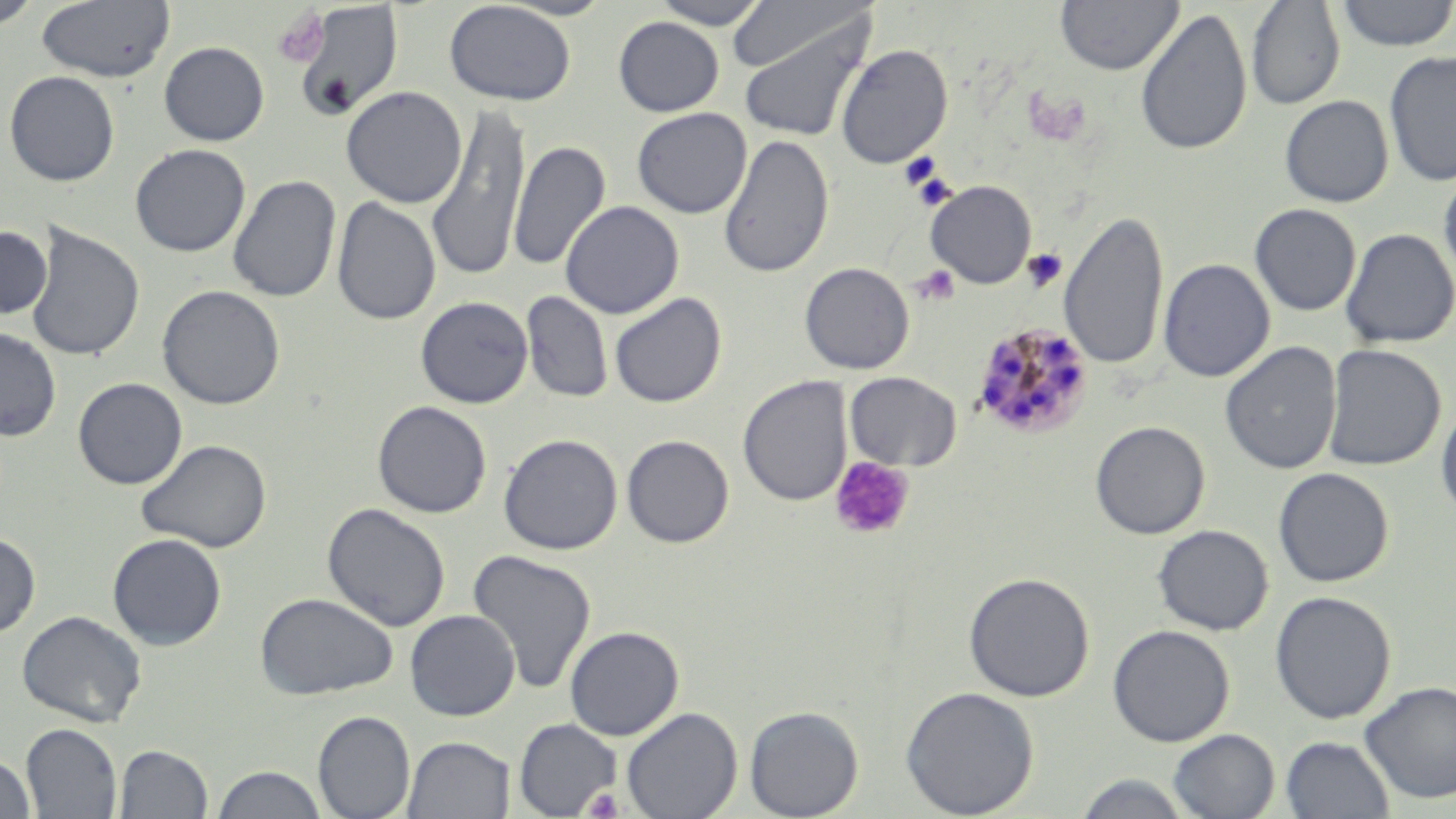
Approximate bounding boxes as (x1, y1, x2, y2) in pixels. Platelet locations: (272, 6, 329, 68), (900, 152, 944, 190), (922, 179, 955, 207), (1022, 249, 1067, 292), (912, 266, 960, 306), (828, 457, 916, 540), (583, 788, 625, 818). Uninfected red blood cell locations: (0, 0, 42, 31), (36, 0, 175, 83), (496, 0, 616, 21), (648, 0, 772, 29), (1055, 0, 1183, 75), (1335, 0, 1456, 51), (444, 1, 576, 106), (727, 1, 870, 75), (1247, 1, 1345, 110), (288, 2, 405, 119), (1135, 8, 1253, 156), (734, 11, 876, 144), (613, 17, 724, 116), (159, 41, 269, 146), (835, 43, 953, 169), (1384, 51, 1456, 187), (3, 70, 120, 186), (340, 86, 467, 208), (1280, 95, 1394, 207), (426, 103, 532, 281), (632, 107, 752, 219), (718, 134, 834, 278), (508, 141, 610, 270), (130, 143, 251, 257), (1438, 167, 1456, 290), (227, 175, 341, 303), (924, 180, 1037, 289), (332, 197, 440, 326), (559, 200, 684, 319), (1249, 203, 1361, 316), (1059, 209, 1169, 371), (25, 223, 146, 363), (0, 226, 52, 319), (1341, 228, 1455, 349), (1158, 258, 1275, 382), (799, 262, 914, 374), (157, 284, 286, 410), (521, 291, 613, 403), (609, 293, 726, 408), (415, 296, 534, 409), (0, 327, 61, 441), (1220, 341, 1342, 474), (1322, 344, 1446, 471), (845, 372, 962, 471), (737, 376, 852, 507), (72, 377, 188, 490), (1436, 400, 1456, 521), (372, 401, 491, 518), (1089, 420, 1210, 540), (498, 433, 623, 555), (621, 434, 734, 548), (135, 439, 272, 554), (1273, 467, 1395, 588), (322, 503, 450, 632), (1152, 524, 1274, 635), (0, 531, 41, 638), (107, 533, 227, 650), (467, 549, 597, 694), (962, 571, 1095, 702), (1269, 590, 1397, 724), (254, 592, 397, 700), (405, 609, 520, 721), (17, 610, 147, 727), (564, 625, 684, 740), (1107, 625, 1235, 747), (1359, 680, 1456, 805), (900, 685, 1040, 818), (744, 705, 864, 819), (621, 706, 743, 819), (312, 710, 415, 819), (513, 718, 622, 817), (21, 723, 122, 818), (1168, 729, 1280, 818), (402, 735, 515, 819), (1280, 735, 1394, 819), (114, 743, 213, 818), (0, 755, 35, 818), (211, 765, 328, 818), (1071, 772, 1198, 817). Plasmodium malariae-infected red blood cell locations: (971, 322, 1095, 440). Slide-level diagnosis: Plasmodium malariae. One field of a larger specimen. Image is 1456×819 pixels. Thin blood film. 1000x magnification. May-Grünwald-Giemsa-stained preparation. Optical microscopy.